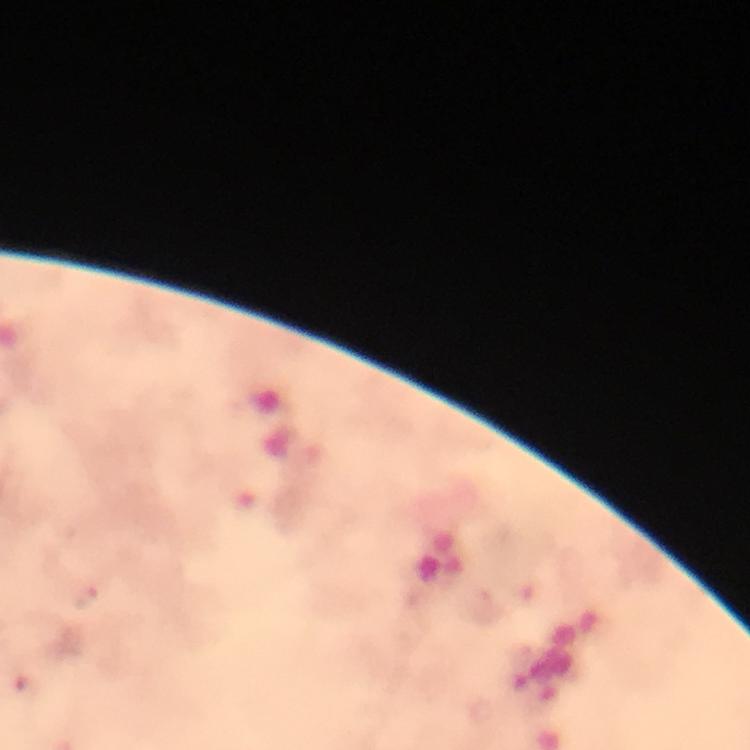
Approximate centers as {x, y} in pixels.
Summary:
  - Plasmodium parasite locations: {86, 599}
  - Preparation: thick blood smear
  - Context: from a diagnostic examination for malaria
  - Cropped from: a single field of view
  - Capture: smartphone camera through the microscope
  - Image size: 750×750 pixels
  - Magnification: 100x
  - Immersion oil: applied
  - Stain: Giemsa